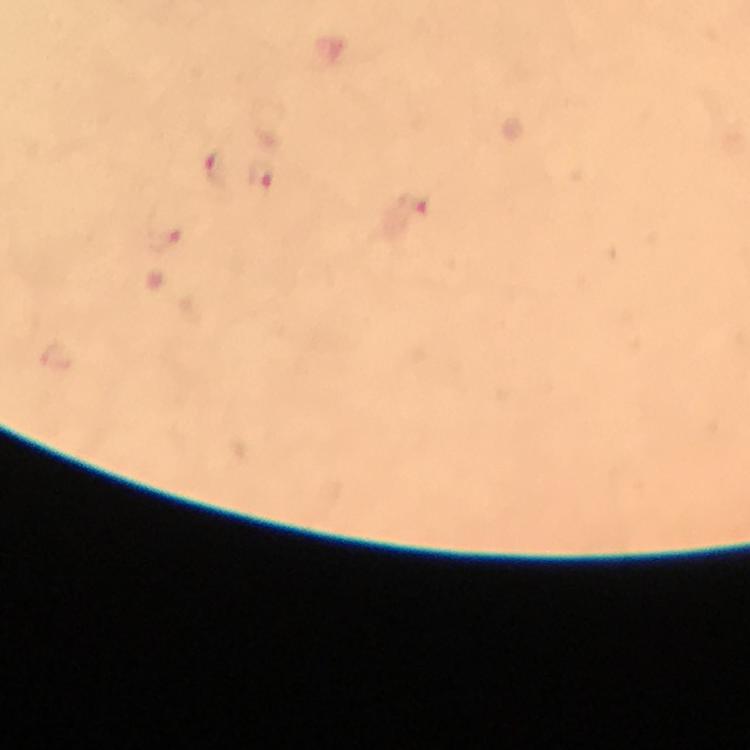
preparation = thick blood film
capture = smartphone mounted on the microscope
image size = 750×750 pixels
immersion oil = used
malaria parasite locations = approximate centers as (x, y) in pixels: (216, 169), (261, 176), (414, 203), (163, 236)
stain = Giemsa
magnification = 100x
cropped from = one field of view
context = from a malaria diagnostic workup